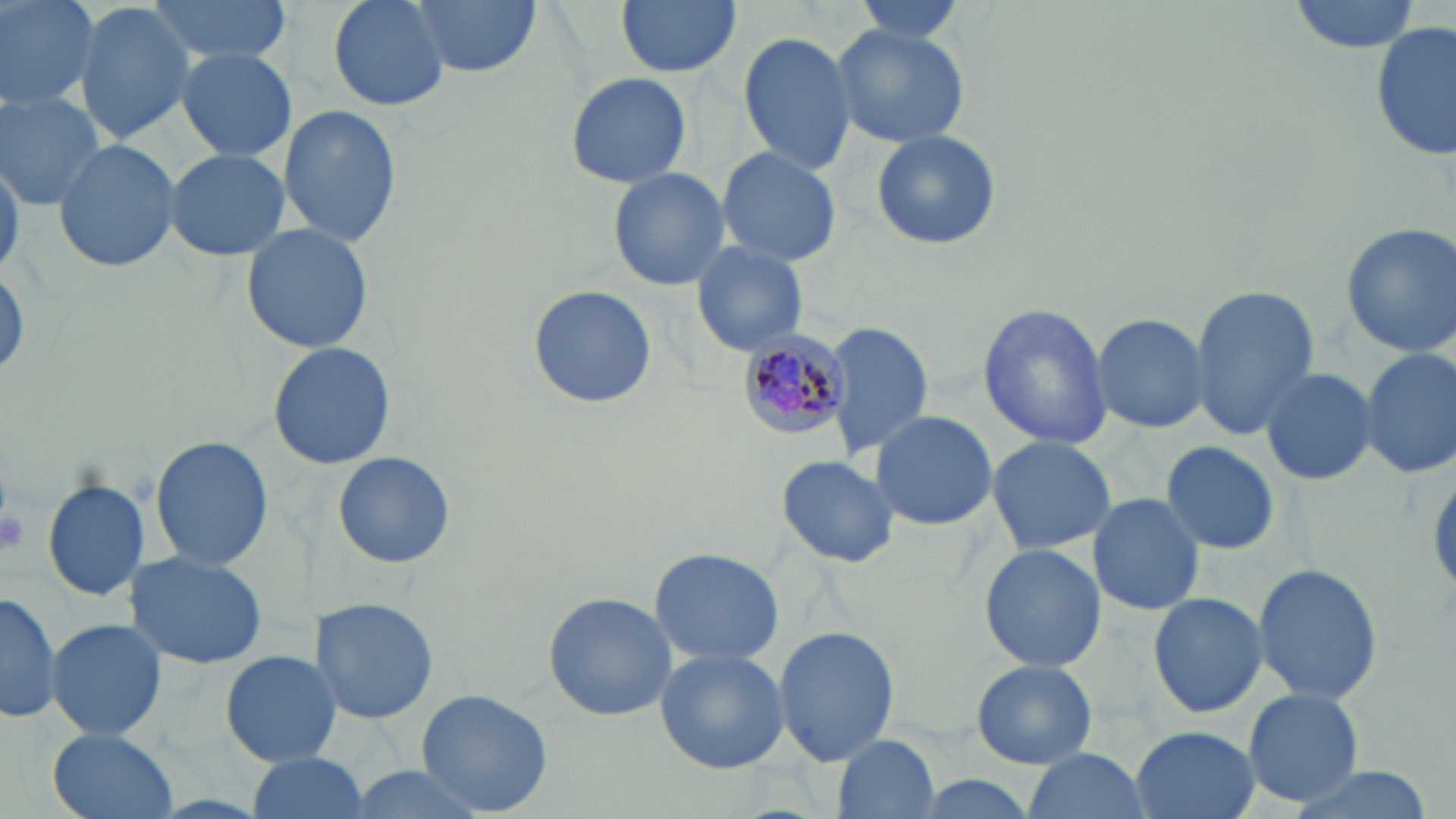 Approximate bounding boxes as named x1/y1/x2/y2 corners in pixels. Platelet locations: (x1=0, y1=501, x2=27, y2=559). Uninfected red blood cell locations: (x1=0, y1=0, x2=101, y2=114), (x1=143, y1=0, x2=300, y2=64), (x1=328, y1=0, x2=450, y2=112), (x1=408, y1=0, x2=542, y2=77), (x1=616, y1=0, x2=740, y2=78), (x1=846, y1=0, x2=970, y2=42), (x1=1288, y1=0, x2=1424, y2=51), (x1=73, y1=2, x2=196, y2=145), (x1=831, y1=22, x2=970, y2=148), (x1=1371, y1=25, x2=1454, y2=160), (x1=737, y1=28, x2=857, y2=178), (x1=174, y1=47, x2=298, y2=164), (x1=564, y1=70, x2=694, y2=187), (x1=0, y1=89, x2=109, y2=208), (x1=277, y1=103, x2=402, y2=250), (x1=870, y1=128, x2=1001, y2=251), (x1=52, y1=136, x2=182, y2=274), (x1=715, y1=145, x2=842, y2=267), (x1=163, y1=146, x2=291, y2=261), (x1=0, y1=150, x2=22, y2=279), (x1=606, y1=167, x2=731, y2=290), (x1=1338, y1=221, x2=1456, y2=358), (x1=240, y1=222, x2=375, y2=356), (x1=691, y1=241, x2=809, y2=356), (x1=526, y1=283, x2=658, y2=410), (x1=1189, y1=285, x2=1319, y2=438), (x1=977, y1=302, x2=1112, y2=450), (x1=1092, y1=313, x2=1208, y2=432), (x1=821, y1=320, x2=936, y2=461), (x1=267, y1=342, x2=396, y2=469), (x1=1358, y1=347, x2=1456, y2=481), (x1=1259, y1=365, x2=1378, y2=487), (x1=870, y1=410, x2=997, y2=533), (x1=985, y1=434, x2=1118, y2=557), (x1=150, y1=435, x2=272, y2=570), (x1=1160, y1=439, x2=1281, y2=556), (x1=332, y1=451, x2=456, y2=569), (x1=776, y1=454, x2=899, y2=568), (x1=42, y1=479, x2=151, y2=603), (x1=1087, y1=493, x2=1206, y2=614), (x1=978, y1=543, x2=1105, y2=674), (x1=650, y1=546, x2=782, y2=668), (x1=126, y1=550, x2=267, y2=669), (x1=1250, y1=563, x2=1384, y2=703), (x1=0, y1=590, x2=63, y2=724), (x1=1149, y1=591, x2=1269, y2=720), (x1=543, y1=592, x2=678, y2=721), (x1=312, y1=597, x2=440, y2=722), (x1=45, y1=618, x2=167, y2=742), (x1=772, y1=625, x2=900, y2=766), (x1=654, y1=648, x2=788, y2=773), (x1=222, y1=650, x2=341, y2=767), (x1=971, y1=659, x2=1098, y2=769), (x1=414, y1=686, x2=554, y2=817), (x1=1243, y1=688, x2=1365, y2=807), (x1=1130, y1=726, x2=1259, y2=819), (x1=44, y1=728, x2=184, y2=819), (x1=832, y1=732, x2=939, y2=817), (x1=1022, y1=748, x2=1151, y2=819), (x1=243, y1=752, x2=372, y2=818), (x1=1277, y1=765, x2=1439, y2=819). Plasmodium malariae-infected red blood cell locations: (x1=732, y1=330, x2=853, y2=442). Slide-level diagnosis: Plasmodium malariae. Thin blood film. Image is 1456×819 pixels. Optical microscopy. Captured at 1000x magnification. May-Grünwald-Giemsa stain. Single field of view.